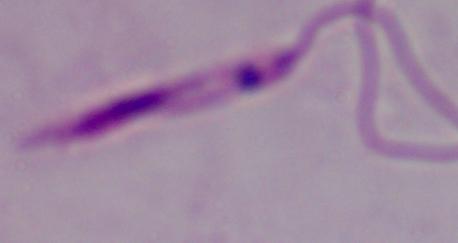
A Leishmania parasite is shown. Photomicrograph. Captured at 1000x magnification.